Identify the blood parasite species.
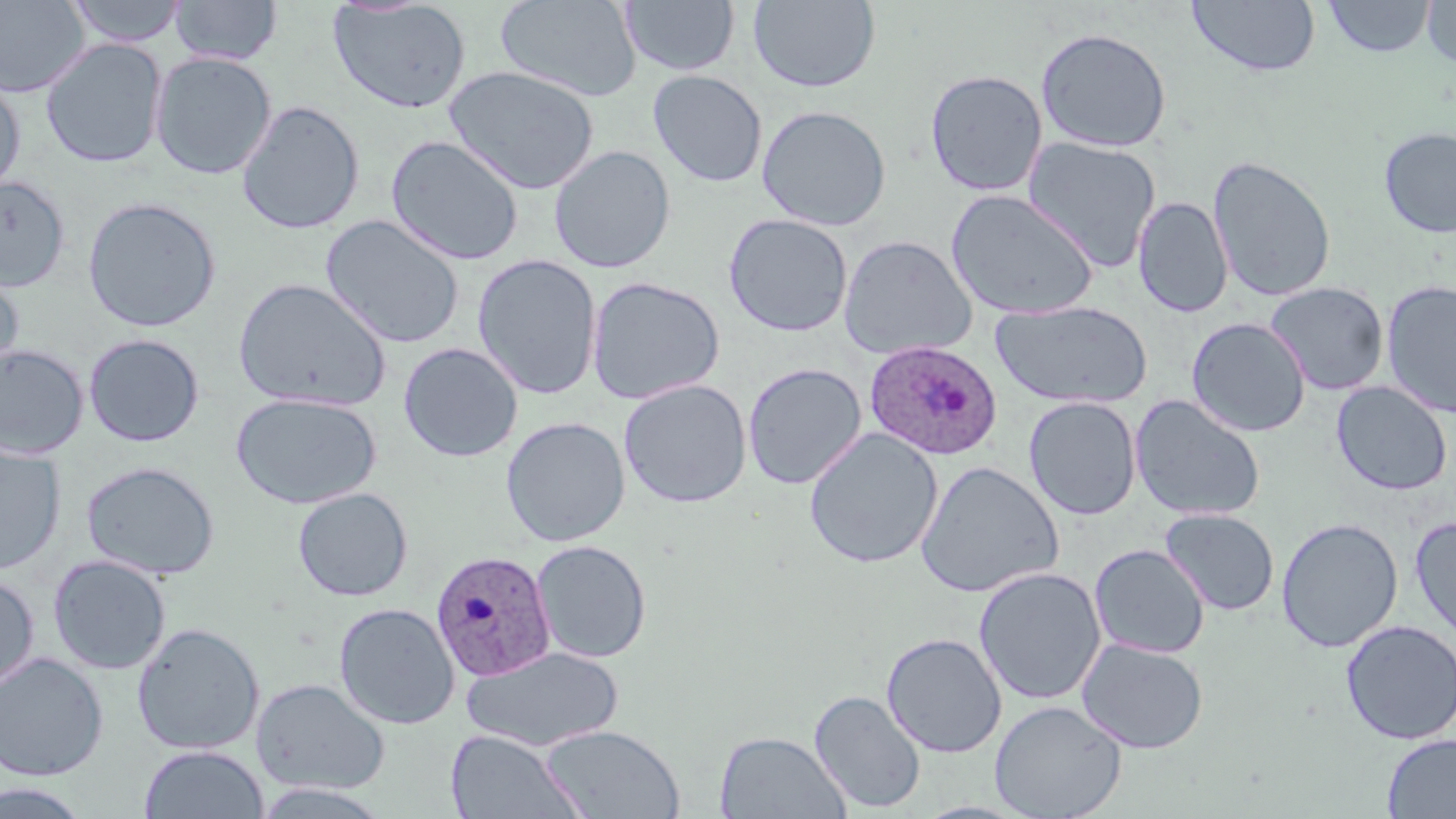

Plasmodium ovale.

Summary:
  - Coordinate format: approximate bounding boxes as (x1,y1)-(x2,y2) corner pairs in pixels
  - Uninfected red blood cell locations: (65,0)-(188,47), (328,0)-(471,114), (496,0)-(642,102), (620,0)-(739,76), (748,0)-(881,93), (1187,0)-(1321,78), (1323,0)-(1436,58), (0,1)-(91,98), (169,1)-(283,65), (1422,1)-(1455,71), (1036,26)-(1172,153), (40,38)-(168,168), (150,52)-(277,180), (444,66)-(600,195), (924,69)-(1048,197), (648,70)-(768,187), (0,74)-(25,197), (236,100)-(365,235), (756,105)-(892,231), (1378,127)-(1456,239), (386,135)-(524,266), (1022,136)-(1161,272), (549,145)-(676,273), (1208,156)-(1337,302), (0,174)-(70,291), (946,189)-(1099,320), (1133,196)-(1233,318), (82,197)-(221,333), (723,213)-(853,337), (321,214)-(465,349), (839,235)-(977,360), (472,254)-(603,400), (0,264)-(24,382), (586,276)-(726,404), (233,277)-(392,412), (1381,280)-(1456,419), (1265,282)-(1390,395), (990,300)-(1153,409), (1186,317)-(1311,437), (84,333)-(205,447), (398,342)-(523,462), (0,344)-(90,460), (742,363)-(867,489), (618,379)-(752,509), (1331,381)-(1452,496), (231,392)-(382,509), (1129,395)-(1266,522), (1023,396)-(1142,520), (500,416)-(631,547), (804,428)-(943,569), (0,445)-(66,575), (81,461)-(220,580), (915,461)-(1064,598), (292,487)-(413,601), (1159,509)-(1279,616), (1410,515)-(1456,645), (1276,517)-(1403,652), (531,539)-(652,664), (1089,543)-(1211,659), (48,555)-(172,675), (973,566)-(1106,705), (0,572)-(39,692), (334,602)-(460,729), (1340,620)-(1455,744), (131,622)-(265,754), (881,632)-(1007,757), (1077,638)-(1209,754), (461,645)-(622,751), (0,653)-(108,780), (251,677)-(390,795), (809,689)-(926,813), (989,700)-(1127,819), (539,725)-(686,818), (446,729)-(586,818), (715,730)-(850,818), (1382,733)-(1456,818), (139,744)-(268,819), (0,780)-(93,818)
  - Plasmodium ovale-infected red blood cell locations: (864,341)-(1003,460), (429,549)-(556,681)
  - Image size: 1456×819 pixels
  - Stain: May-Grünwald-Giemsa
  - Magnification: 1000x
  - Field of view: one of a larger specimen
  - Preparation: thin blood smear
  - Modality: light microscopy